Locate every malaria parasite and every leukocyte.
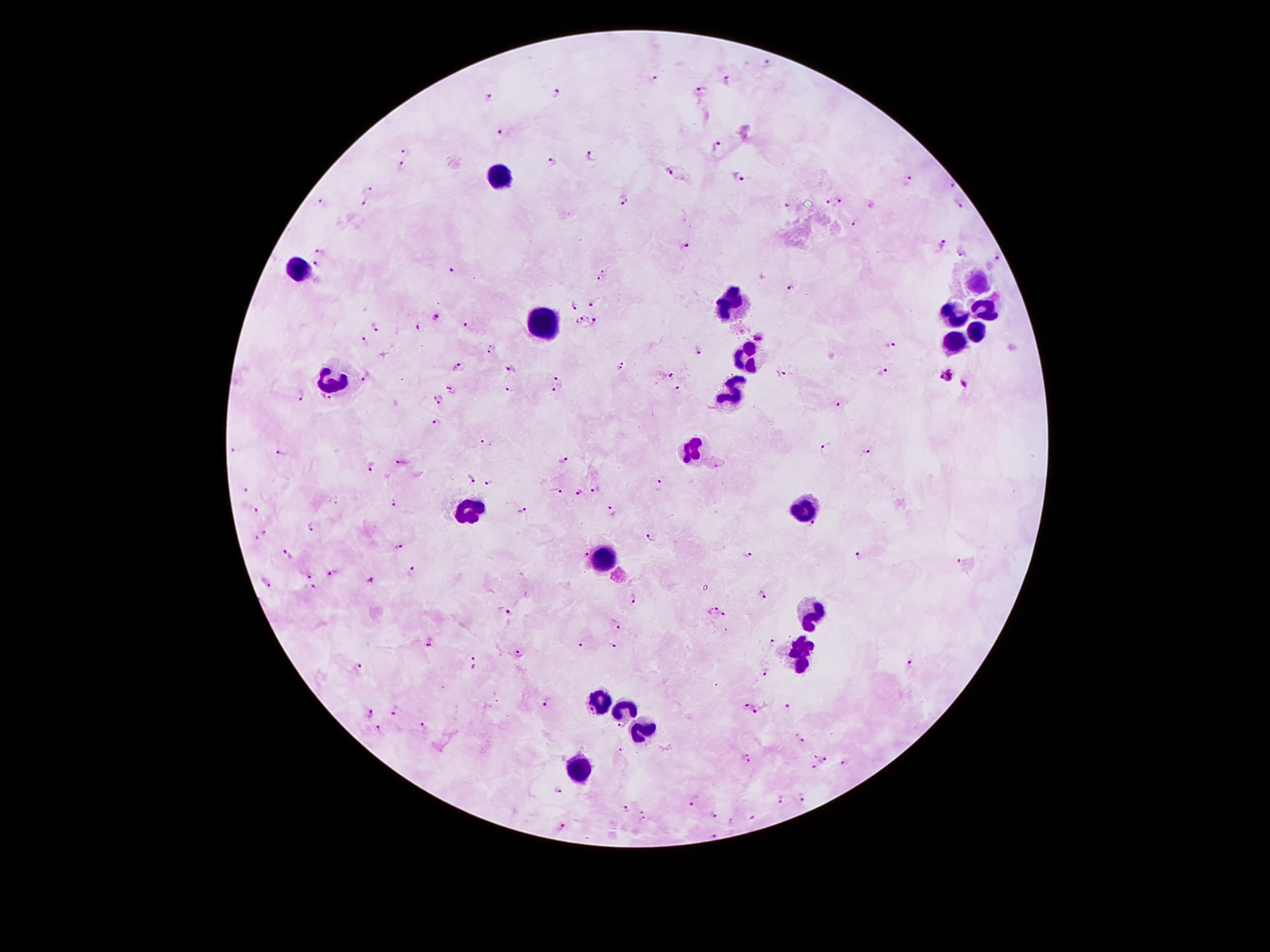

Approximate centers as [x, y] in pixels.
Malaria parasites: [768, 64], [653, 80], [726, 80], [701, 91], [555, 94], [487, 96], [502, 133], [716, 147], [406, 153], [592, 155], [550, 161], [402, 166], [668, 172], [738, 179], [908, 180], [952, 185], [367, 190], [624, 201], [365, 202], [840, 202], [828, 203], [323, 205], [959, 205], [854, 226], [941, 243], [685, 247], [320, 252], [962, 252], [998, 258], [316, 265], [604, 267], [449, 270], [599, 278], [791, 284], [595, 300], [575, 304], [435, 318], [582, 320], [596, 321], [466, 325], [376, 326], [420, 328], [759, 338], [365, 341], [892, 346], [492, 349], [696, 352], [620, 365], [457, 367], [512, 367], [883, 371], [670, 372], [781, 375], [946, 375], [367, 377], [557, 379], [963, 383], [677, 386], [452, 390], [556, 390], [508, 393], [438, 396], [302, 397], [324, 400], [838, 404], [435, 421], [484, 443], [825, 447], [234, 452], [866, 452], [281, 453], [401, 461], [563, 462], [371, 467], [470, 479], [490, 483], [660, 486], [246, 489], [596, 490], [556, 491], [579, 493], [335, 499], [396, 503], [256, 510], [523, 511], [610, 512], [312, 528], [264, 534], [652, 536], [258, 538], [399, 547], [288, 554], [749, 555], [582, 556], [861, 556], [956, 561], [412, 571], [333, 572], [309, 574], [370, 580], [267, 583], [310, 586], [762, 597], [634, 600], [712, 610], [505, 612], [726, 614], [619, 627], [429, 641], [772, 642], [582, 644], [613, 645], [519, 654], [475, 662], [912, 664], [359, 665], [765, 673], [548, 702], [746, 705], [786, 708], [394, 709], [759, 711], [369, 712], [621, 726], [421, 728], [379, 729], [801, 739], [621, 747], [748, 758], [824, 758], [845, 763], [812, 766], [559, 789], [800, 798], [781, 799], [694, 800], [625, 811], [643, 814], [714, 814], [751, 817], [561, 828], [715, 836].
Leukocytes: [502, 176], [298, 269], [975, 282], [732, 298], [984, 308], [956, 314], [543, 325], [975, 333], [953, 344], [748, 357], [335, 381], [733, 392], [693, 450], [805, 507], [471, 510], [606, 559], [813, 616], [801, 656], [597, 699], [624, 708], [642, 730], [578, 767].

Summary:
  - Stain: Giemsa
  - Patient malaria status: positive for Plasmodium falciparum
  - Field of view: one from this slide
  - Capture: smartphone camera through the microscope eyepiece
  - Preparation: thick peripheral-blood smear
  - Magnification: 100x
  - Image size: 1270×952 pixels